Assess this cell for malaria.
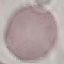
It is uninfected.

{
  "stain": "Giemsa",
  "capture": "smartphone through the microscope eyepiece",
  "image_type": "cell patch, automatically extracted from a larger field of view and resized to 64 × 64 pixels",
  "preparation": "thin smear"
}